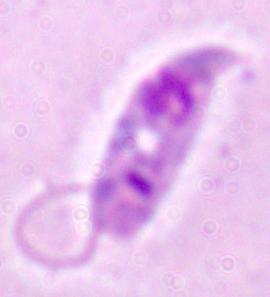
Photomicrograph. 1000x magnification. A Leishmania parasite is seen.